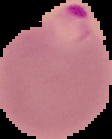

preparation = thin blood smear
image size = 112×139 pixels
malaria status = parasitized
image type = segmented cell region with the area outside set to black